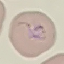

Summary:
  - Result: malaria parasites identified
  - Stain: Giemsa
  - Capture: smartphone camera at the microscope eyepiece
  - Preparation: thin blood film
  - Image type: cell patch, automatically extracted from a larger field of view and resized to 64 × 64 pixels